Assess this cell for malaria.
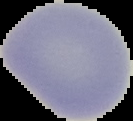
It is uninfected.

{
  "preparation": "thin blood film",
  "image_type": "segmented cell region with the area outside set to black",
  "image_size": "133×121 pixels"
}